State which parasite is depicted.
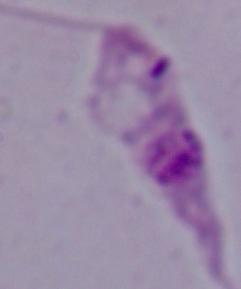

Leishmania.

1000x magnification. Photomicrograph.